Describe the morphology of the erythrocytes.
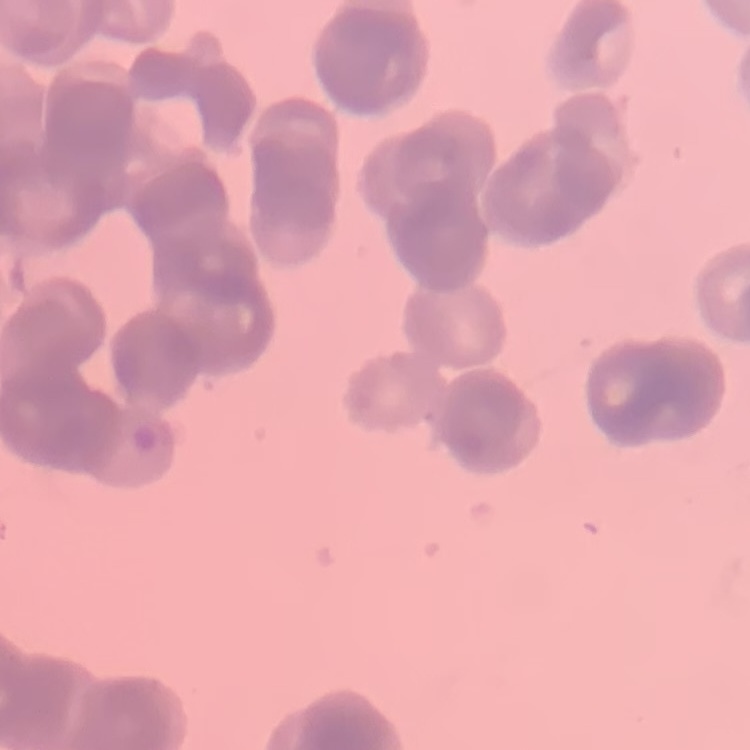
They show rouleaux formation.

Summary:
  - Preparation: thin blood film
  - Image type: square crop of a larger photomicrograph
  - Stain: Field's or Giemsa